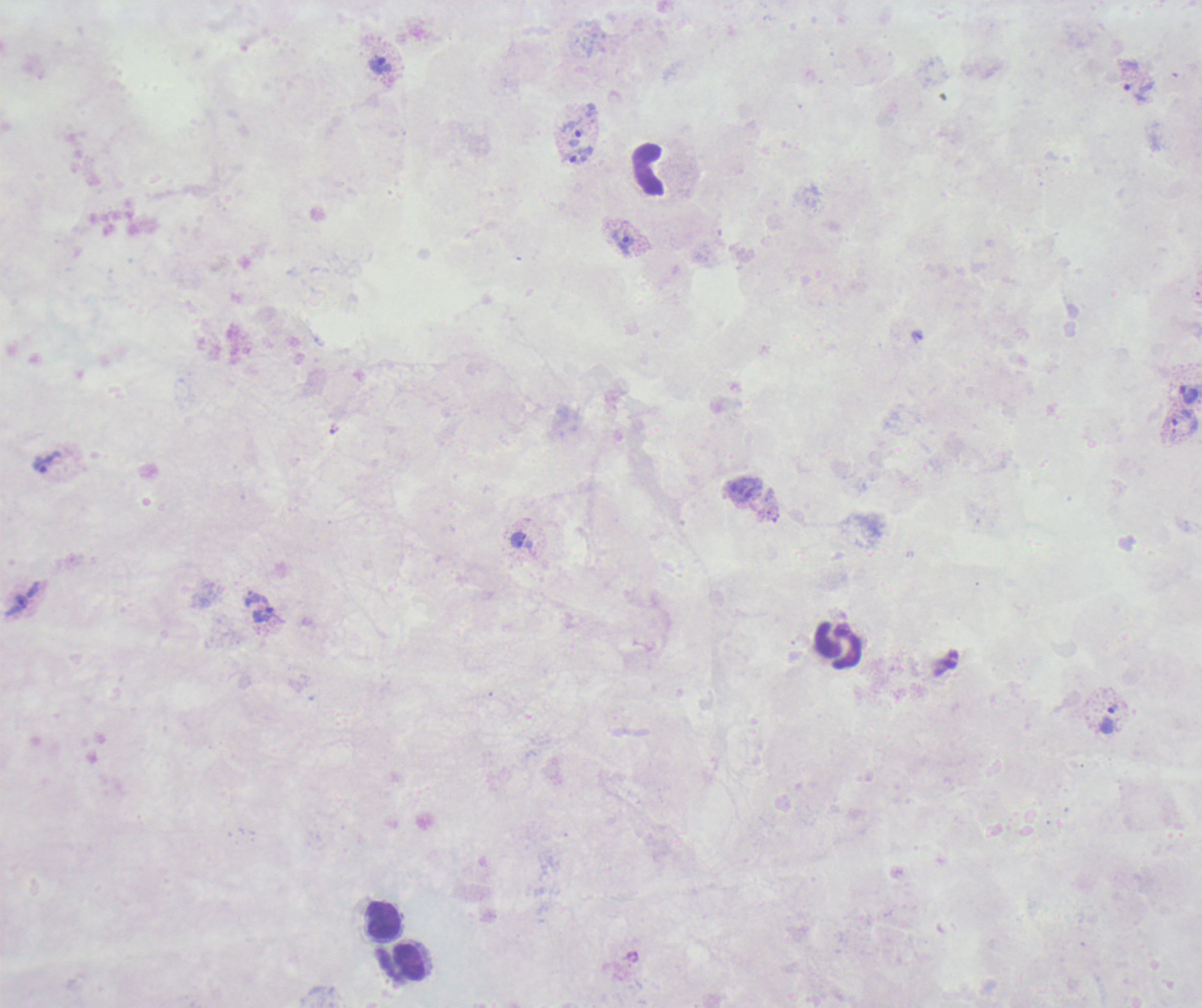

{
  "field_of_view": "single",
  "trophozoite_locations": "approximate object centers, in pixels from the top-left corner: (x=380, y=66), (x=1134, y=94), (x=574, y=137), (x=575, y=156), (x=625, y=242), (x=917, y=336), (x=1188, y=394), (x=1181, y=416), (x=334, y=428), (x=46, y=462), (x=518, y=541), (x=21, y=602), (x=264, y=614), (x=1107, y=721)",
  "coloration_quality": "bad",
  "stain": "Romanowsky",
  "result": "positive for Plasmodium parasites",
  "magnification": "100x",
  "image_size": "1202×1008 pixels",
  "leukocyte_locations": "approximate object centers, in pixels from the top-left corner: (x=649, y=173), (x=839, y=647), (x=383, y=922), (x=412, y=961)",
  "background_quality": "poor",
  "preparation": "thick blood film",
  "context": "previously used in a real diagnosis"
}